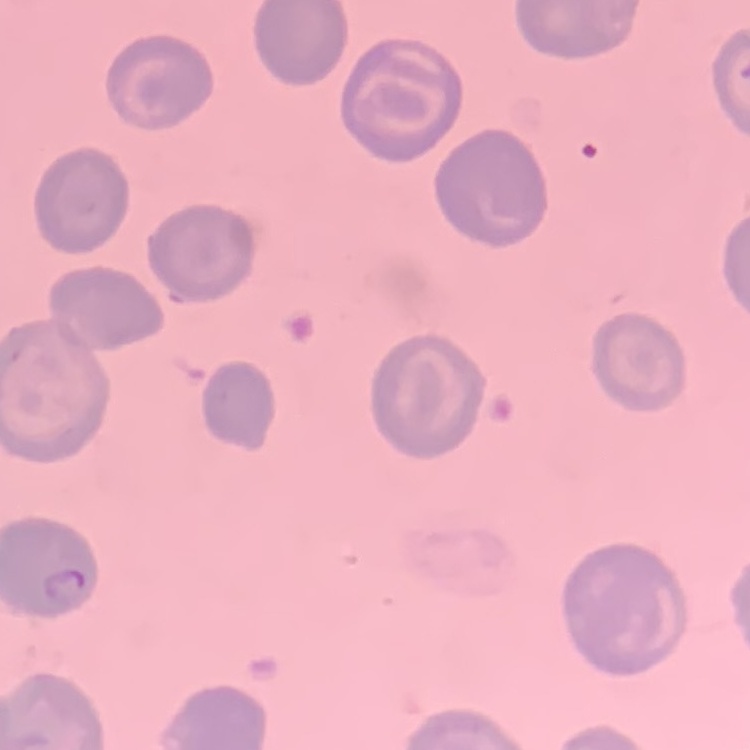 The erythrocytes exhibit no rouleaux formation. Thin blood smear. Field's or Giemsa stain. One tile cut from a larger photomicrograph.